Report the malaria status of this cell.
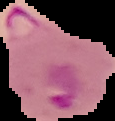
It is parasitized.

Summary:
  - Image size: 115×121 pixels
  - Preparation: thin blood film
  - Image type: cell region segmented out of the field of view; surrounding area masked to black